Describe the morphology of the red blood cells.
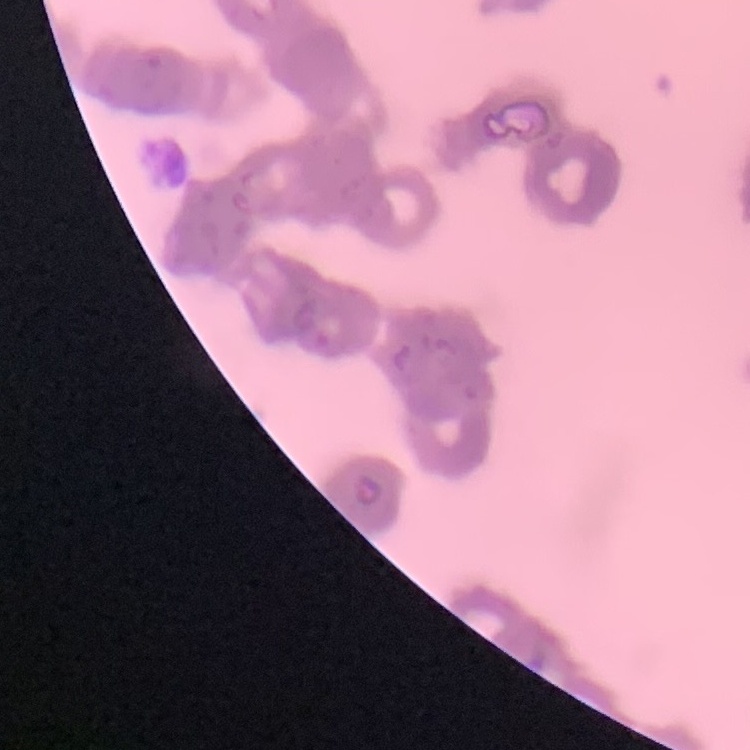
Rouleaux formation.

stain = Field's or Giemsa
preparation = thin blood film
image type = one tile cut from a larger photomicrograph